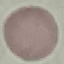

malaria status = uninfected
preparation = thin smear
stain = Giemsa
capture = smartphone through the microscope eyepiece
image type = cell patch, automatically extracted from a larger field of view and resized to 64 × 64 pixels